Assess the morphology of the erythrocytes.
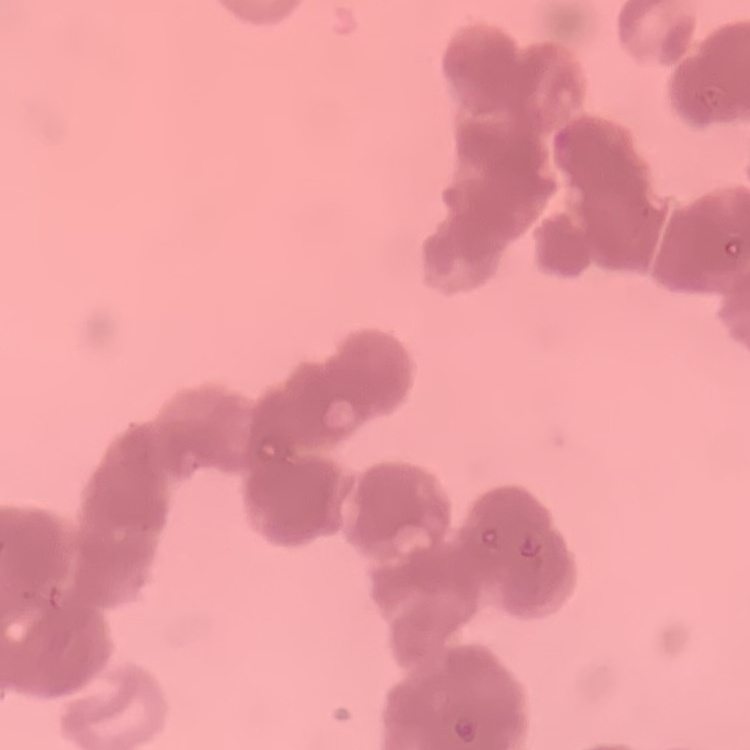
They show rouleaux formation.

stain: Field's or Giemsa
image_type: one tile cut from a larger photomicrograph
preparation: thin blood smear